Assess this cell for malaria.
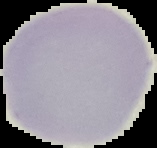

It is uninfected.

{
  "image_type": "segmented cell region on a black background",
  "image_size": "157×148 pixels",
  "preparation": "thin blood film"
}